State the blood parasite species.
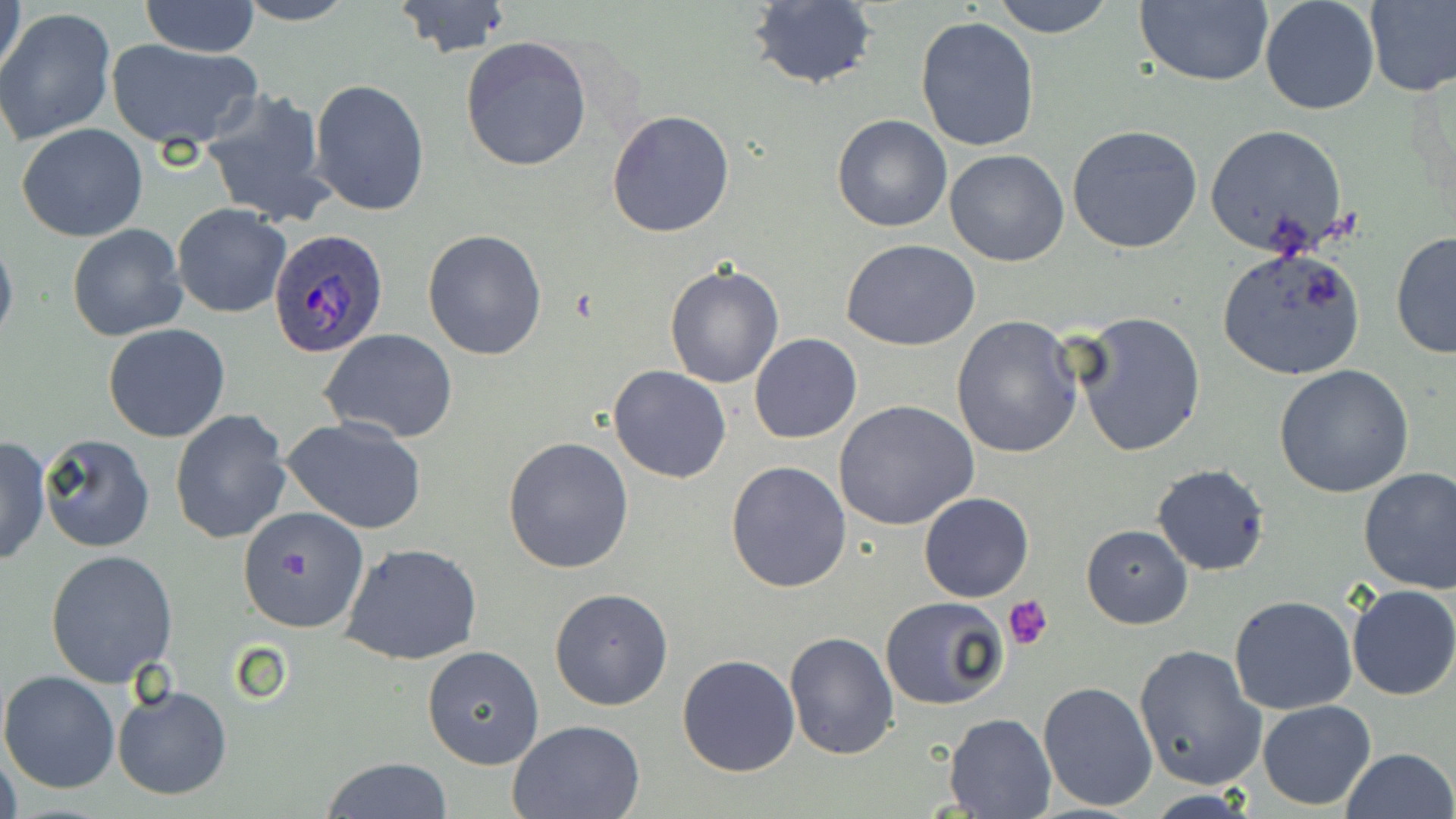
Plasmodium ovale.

Approximate bounding boxes as (x1,y1)-(x2,y2) corner pairs in pixels. Uninfected red blood cell locations: (1,0)-(27,83), (138,0)-(262,57), (990,0)-(1117,39), (1135,0)-(1275,88), (1259,0)-(1379,116), (234,1)-(355,25), (390,1)-(514,59), (745,1)-(880,90), (1365,1)-(1456,97), (2,8)-(116,145), (915,17)-(1040,154), (461,35)-(592,173), (105,37)-(261,150), (310,79)-(431,218), (201,88)-(334,226), (607,110)-(735,238), (832,113)-(952,234), (16,123)-(148,242), (1067,123)-(1204,252), (1205,123)-(1351,259), (943,149)-(1070,267), (171,204)-(291,318), (67,223)-(187,342), (422,229)-(547,360), (0,230)-(18,351), (1390,230)-(1455,360), (840,239)-(981,351), (1216,246)-(1367,380), (663,263)-(784,390), (1072,309)-(1206,457), (949,315)-(1085,458), (103,324)-(231,443), (320,328)-(459,444), (749,334)-(861,443), (1275,365)-(1414,500), (607,366)-(731,483), (834,400)-(979,532), (169,409)-(292,545), (280,416)-(429,534), (38,433)-(157,552), (503,436)-(635,574), (0,437)-(51,566), (725,460)-(852,593), (1152,464)-(1271,576), (1358,467)-(1456,594), (919,491)-(1033,602), (236,505)-(369,633), (1082,526)-(1193,629), (339,541)-(483,666), (46,550)-(179,687), (1347,583)-(1456,701), (550,589)-(674,710), (880,595)-(1011,711), (1229,595)-(1359,715), (785,630)-(899,760), (1133,642)-(1267,792), (422,645)-(544,769), (677,654)-(800,776), (0,671)-(121,793), (1038,681)-(1157,811), (113,684)-(233,801), (1258,699)-(1376,809), (944,712)-(1054,817), (507,719)-(646,818), (0,747)-(22,819), (1341,747)-(1455,819), (320,758)-(454,817). Plasmodium ovale-infected red blood cell locations: (267,228)-(390,360). Platelet locations: (1004,594)-(1054,652). Single field of view. Captured at 1000x magnification. May-Grünwald-Giemsa stain. Image is 1456×819 pixels. Optical microscopy. Thin blood film.